Classify this cell by malaria status.
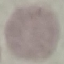

Uninfected.

preparation: thin smear
stain: Giemsa
capture: smartphone through the microscope eyepiece
image_type: automatically extracted cell patch, resized to 64 × 64 pixels